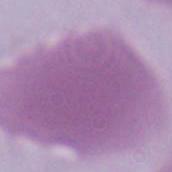
{
  "identification": "erythrocyte",
  "modality": "micrograph",
  "magnification": "1000x"
}